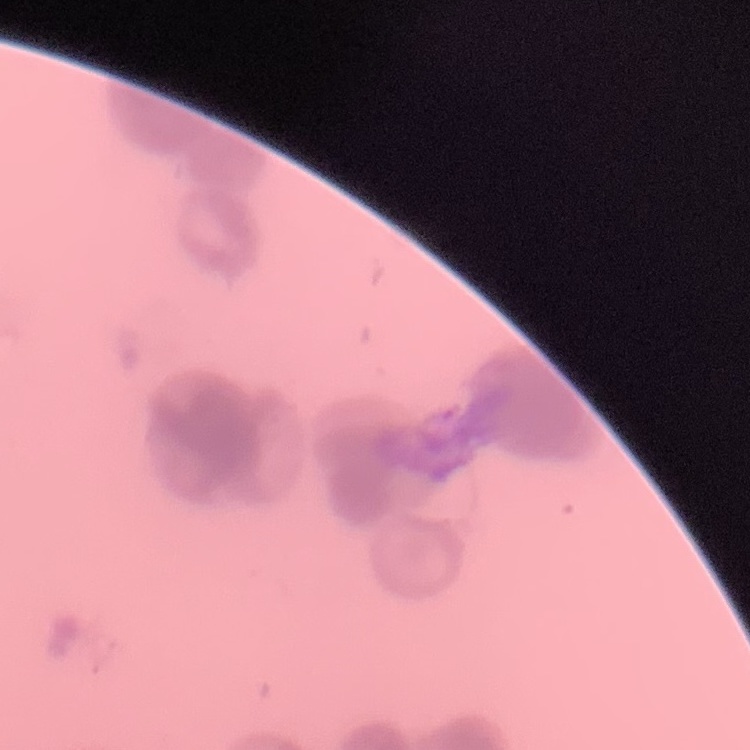 The red blood cells exhibit rouleaux formation. Stained with either Field's or Giemsa. Thin blood film. One tile cut from a larger photomicrograph.